Comment on the morphology of the red blood cells.
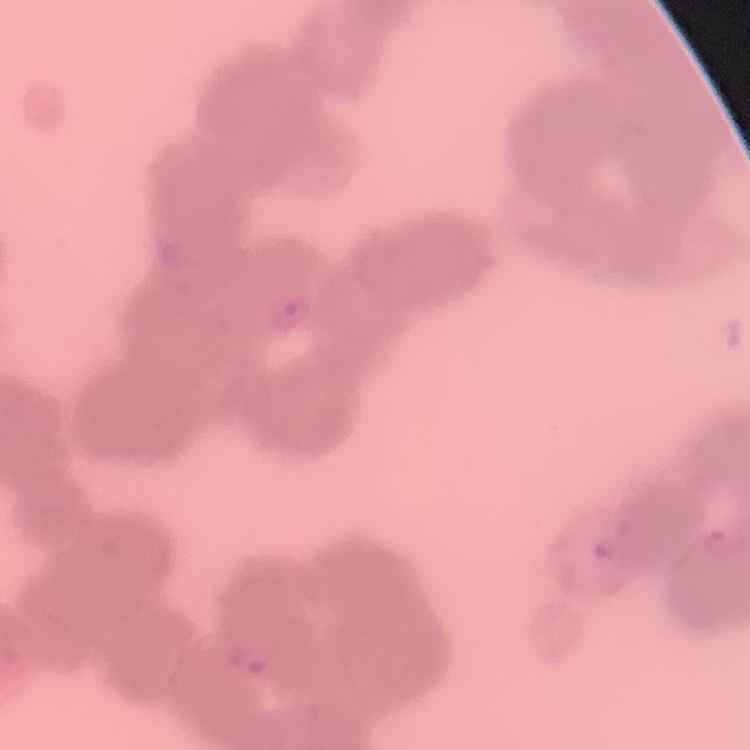
Rouleaux formation.

preparation = thin peripheral smear
image type = one tile cut from a larger photomicrograph
stain = Field's or Giemsa